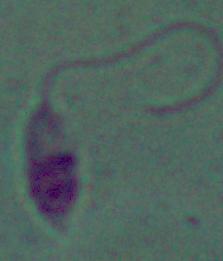

Summary:
  - Identification: Leishmania
  - Magnification: 1000x
  - Modality: micrograph